State which parasite is depicted.
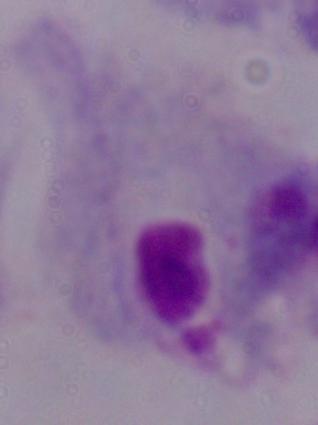

This is a trichomonad.

magnification: 1000x
modality: photomicrograph